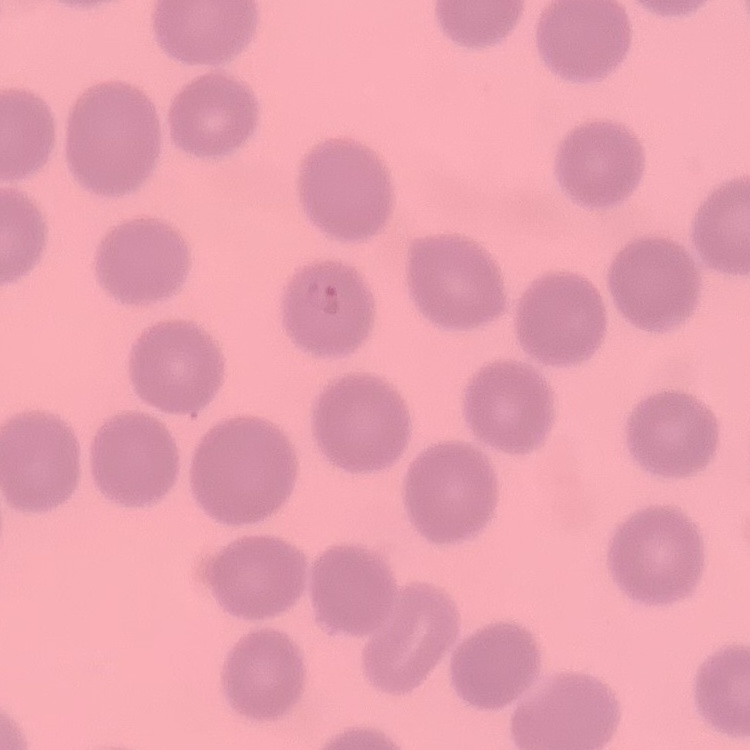 The red blood cells show no rouleaux formation. Field's or Giemsa stain. Square crop of a larger photomicrograph. Thin blood smear.